Assess the morphology of the erythrocytes.
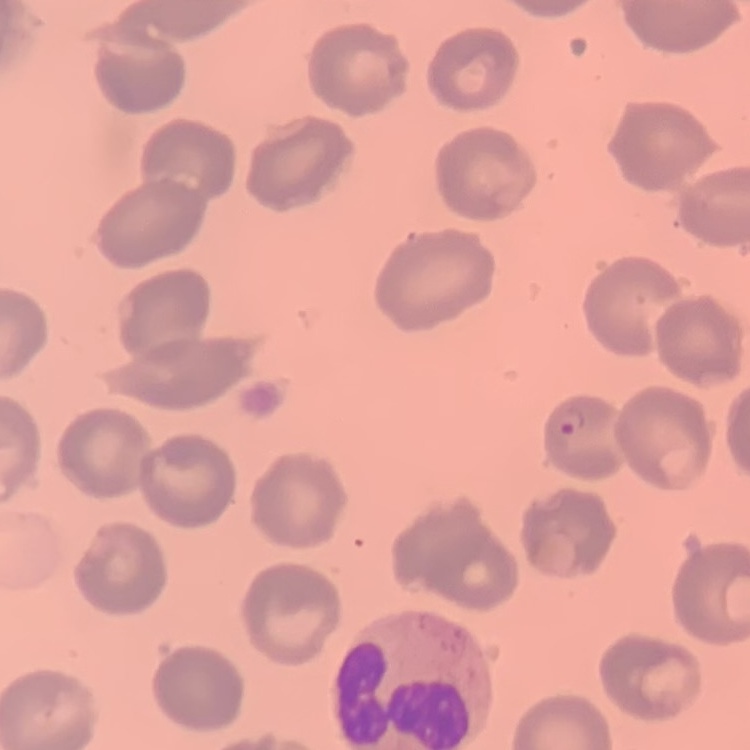
They show no rouleaux formation.

stain = Field's or Giemsa
image type = one tile cut from a larger photomicrograph
preparation = thin peripheral smear